Classify this cell by malaria status.
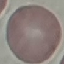
Uninfected.

Thin smear of blood. Automatically extracted cell patch, resized to 64 × 64 pixels. Photographed with a smartphone camera at the microscope eyepiece. Giemsa stain.